Locate every malaria parasite and every leukocyte.
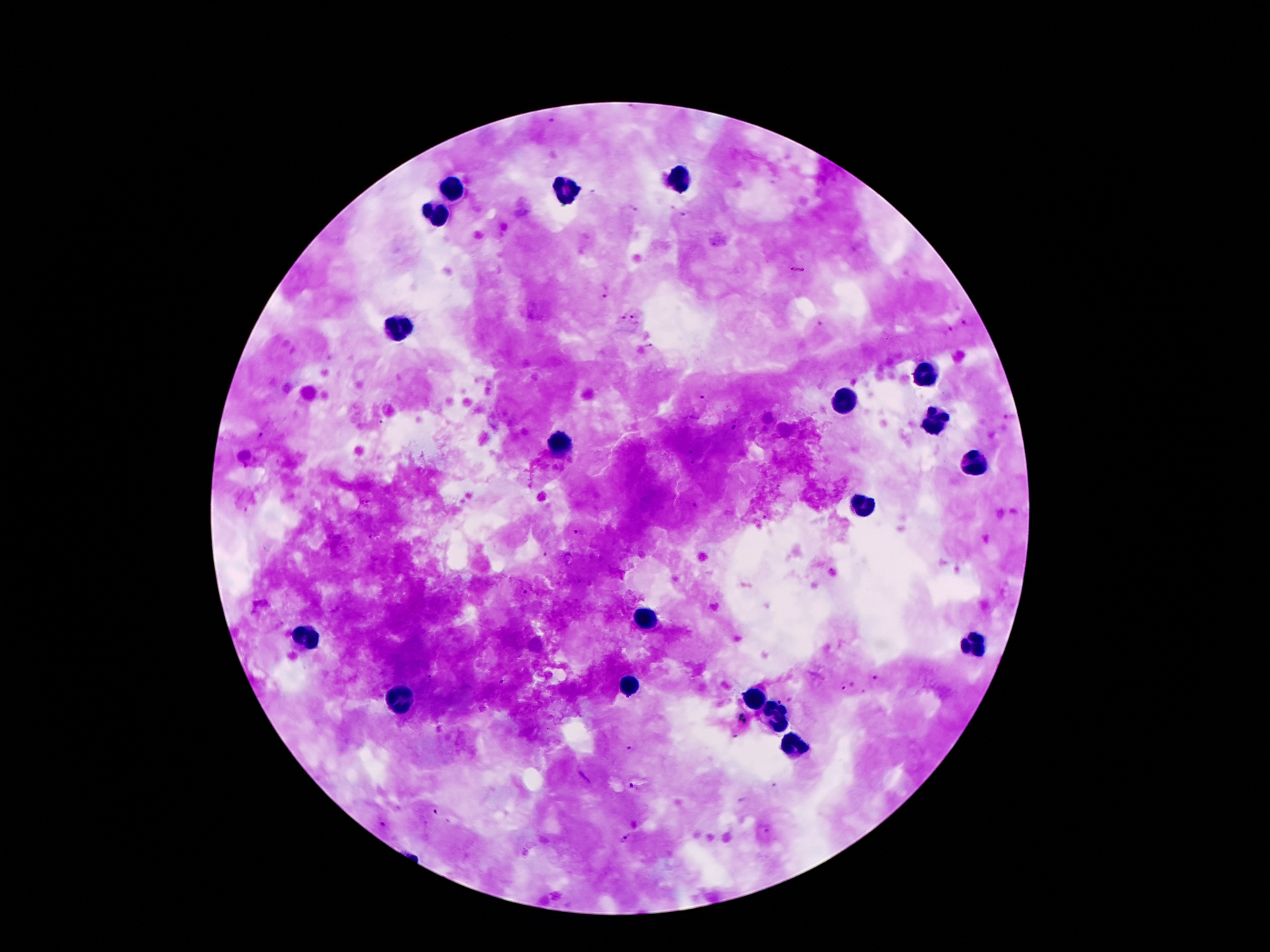

Approximate centers as (x, y) in pixels.
Malaria parasites: (552, 118), (633, 209), (684, 218), (797, 270), (606, 291), (634, 318), (620, 319), (820, 324), (964, 324), (950, 328), (649, 346), (702, 398), (1009, 418), (735, 430), (261, 435), (691, 450), (693, 464), (245, 510), (576, 532), (370, 539), (543, 554), (580, 581), (523, 591), (430, 678), (877, 678), (501, 681), (852, 683), (839, 690), (864, 693), (743, 719), (632, 748), (634, 788), (435, 812), (383, 824), (763, 831), (624, 840).
Leukocytes: (685, 179), (454, 188), (566, 192), (439, 212), (397, 330), (925, 373), (842, 399), (935, 418), (556, 443), (973, 462), (866, 511), (649, 620), (304, 638), (973, 645), (631, 687), (754, 701), (398, 704), (773, 715), (796, 752).

Giemsa-stained preparation. 100x magnification. Thick blood film. Photographed through the microscope eyepiece with a smartphone camera. Patient malaria status: positive for Plasmodium falciparum. Single field of view. Image is 1270×952 pixels.